Describe the morphology of the red blood cells.
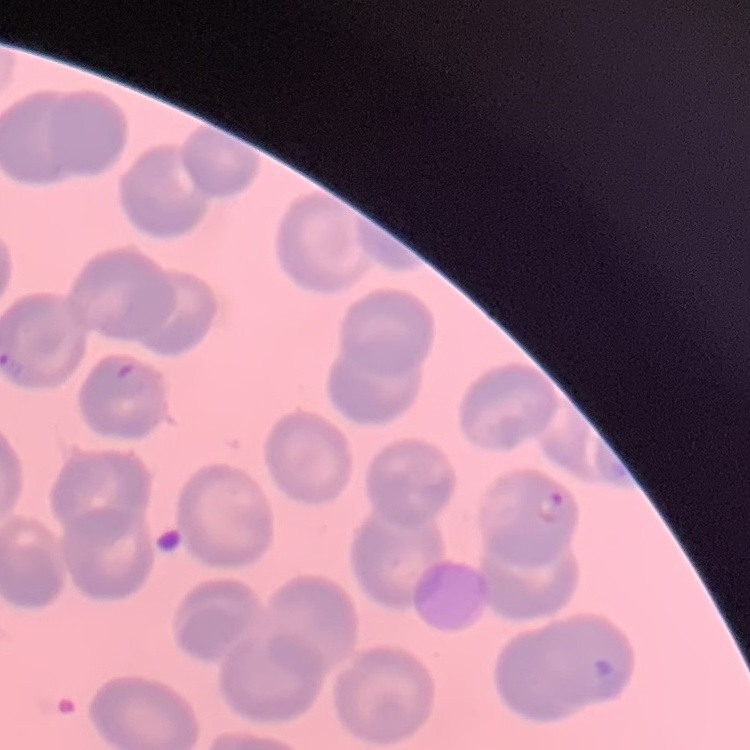

They show no rouleaux formation.

Thin peripheral smear. Square crop of a larger photomicrograph. Field's or Giemsa stain.